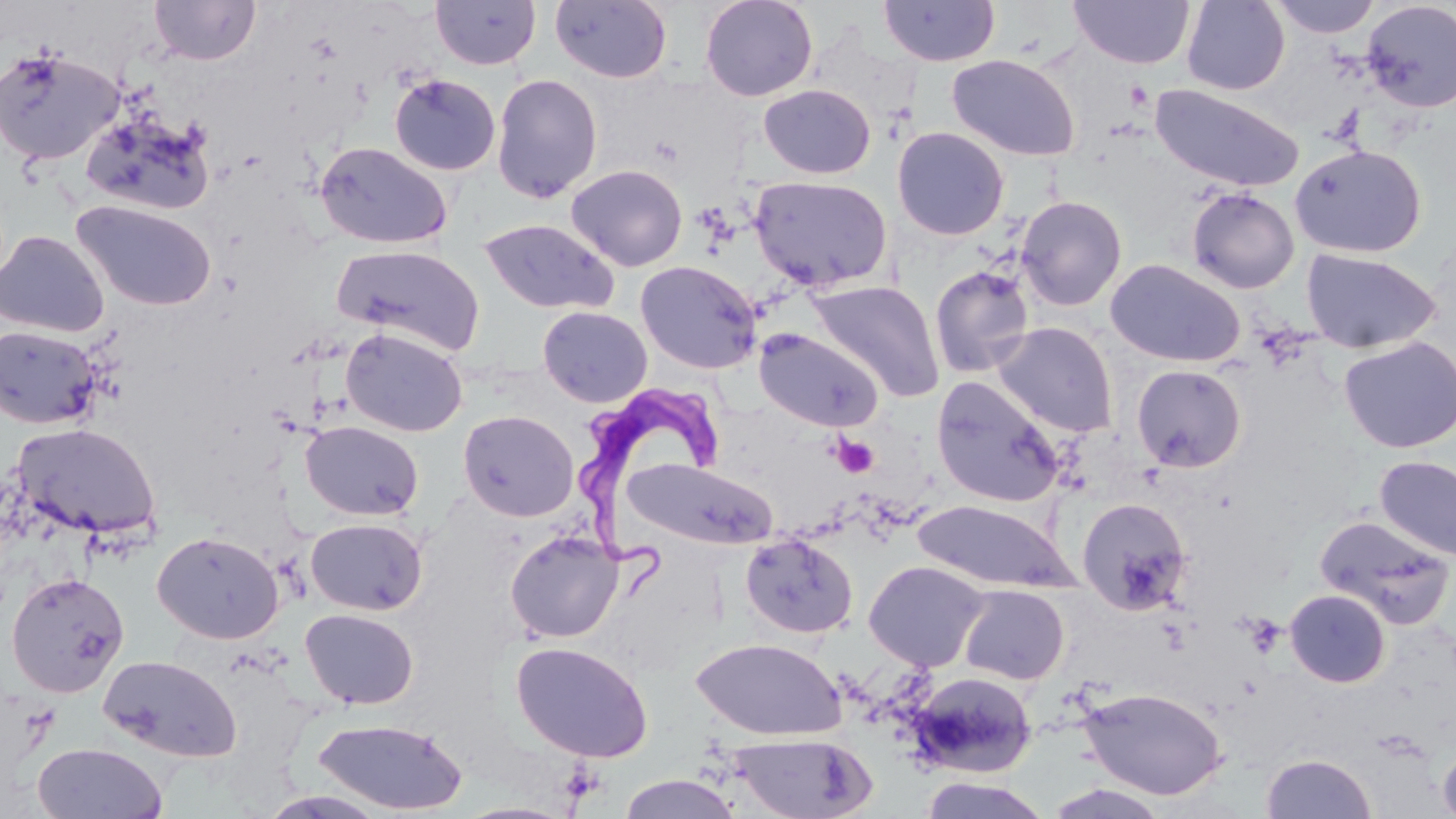

Approximate bounding boxes as (x1, y1, x2, y2) in pixels. Platelet locations: (832, 436, 879, 478). Uninfected red blood cell locations: (150, 0, 260, 65), (430, 0, 541, 70), (550, 0, 673, 84), (700, 0, 818, 102), (1069, 0, 1195, 69), (1181, 0, 1290, 95), (1270, 0, 1382, 38), (878, 1, 1000, 66), (1360, 1, 1456, 113), (0, 44, 125, 167), (946, 53, 1081, 161), (491, 73, 603, 203), (389, 74, 500, 176), (1149, 82, 1306, 194), (758, 84, 876, 179), (81, 110, 217, 217), (892, 127, 1010, 240), (314, 141, 452, 249), (1290, 144, 1427, 258), (565, 163, 688, 272), (749, 175, 894, 292), (1186, 188, 1300, 294), (1015, 195, 1127, 311), (72, 200, 217, 312), (479, 218, 619, 316), (0, 230, 110, 338), (332, 243, 485, 356), (1301, 248, 1441, 354), (1105, 259, 1246, 367), (635, 260, 762, 374), (929, 265, 1036, 379), (807, 280, 944, 402), (537, 306, 653, 407), (992, 321, 1119, 437), (0, 325, 102, 430), (340, 327, 468, 437), (754, 328, 884, 432), (1338, 336, 1455, 454), (1131, 364, 1247, 472), (931, 375, 1065, 508), (458, 409, 578, 521), (301, 420, 423, 521), (12, 422, 162, 540), (1374, 455, 1456, 563), (626, 458, 778, 549), (1075, 497, 1193, 614), (911, 500, 1079, 592), (1315, 515, 1454, 630), (305, 517, 428, 615), (505, 530, 623, 643), (152, 531, 284, 644), (740, 533, 859, 639), (864, 560, 990, 672), (6, 571, 129, 697), (959, 584, 1069, 684), (1285, 589, 1391, 687), (300, 608, 419, 710), (691, 637, 846, 741), (511, 641, 653, 761), (98, 655, 242, 762), (909, 670, 1038, 778), (1077, 685, 1228, 800), (312, 718, 469, 814), (729, 733, 877, 819), (1437, 740, 1456, 819), (32, 742, 169, 818), (1261, 753, 1376, 818), (616, 774, 745, 818), (918, 775, 1051, 819). Trypanosoma brucei locations: (574, 380, 720, 599). Slide-level diagnosis: Trypanosoma brucei. Thin blood smear. May-Grünwald-Giemsa-stained preparation. Image is 1456×819 pixels. Captured at 1000x magnification. Optical microscopy. One field of a larger specimen.